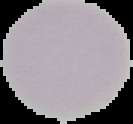
Summary:
  - Image size: 133×124 pixels
  - Preparation: thin blood film
  - Image type: cell region segmented out of the field of view; surrounding area masked to black
  - Malaria status: uninfected